Name the parasite shown.
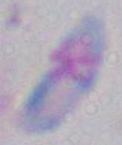
This is Toxoplasma gondii.

Summary:
  - Modality: photomicrograph
  - Magnification: 1000x